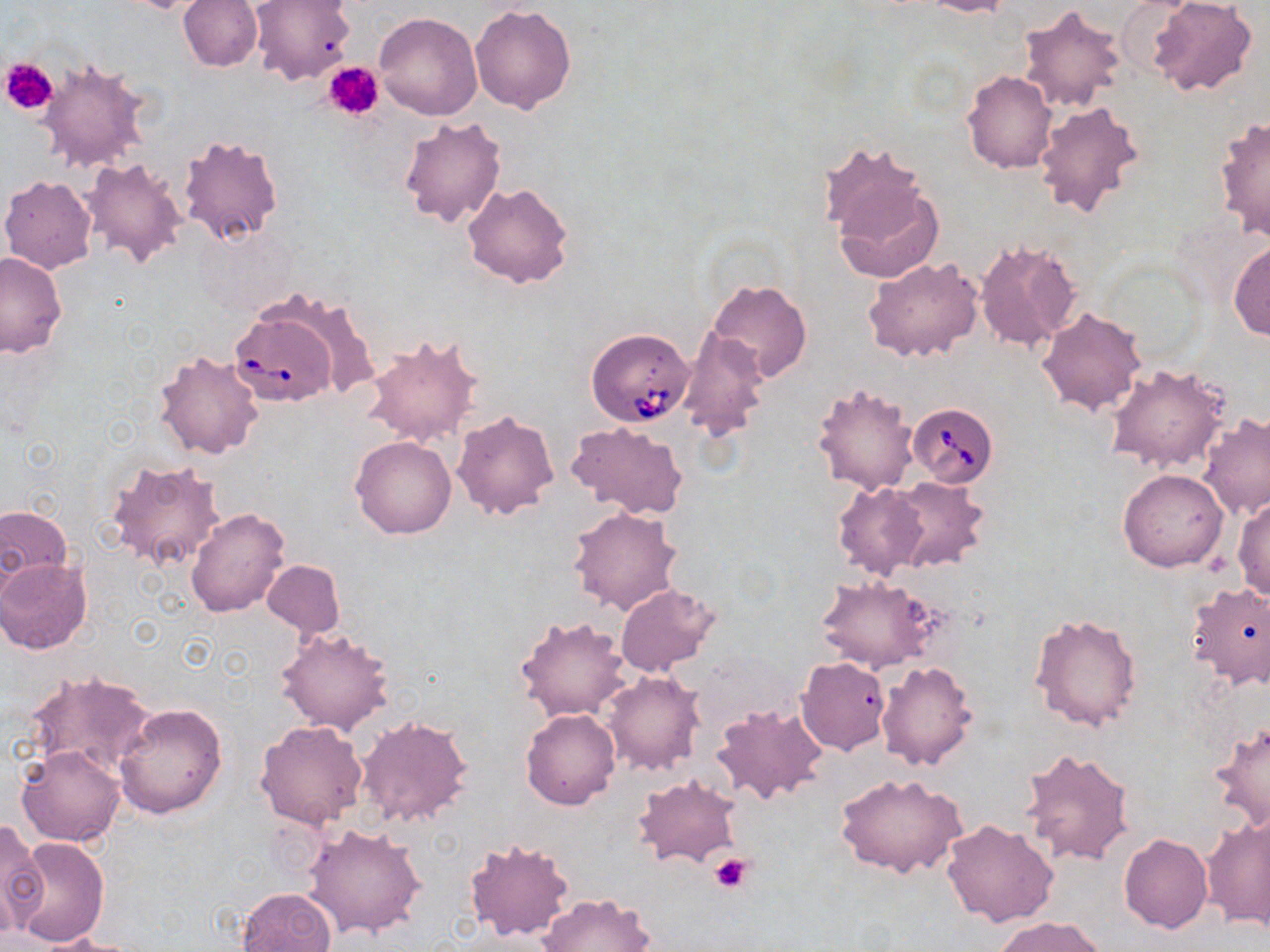 Approximate bounding boxes as (x1, y1, x2, y2) in pixels. Babesia divergens-infected red blood cell locations: (230, 307, 338, 408), (586, 327, 694, 429), (908, 402, 999, 487). Uninfected red blood cell locations: (178, 0, 261, 72), (251, 0, 357, 86), (922, 0, 1011, 17), (1115, 1, 1193, 74), (1148, 1, 1256, 97), (469, 4, 577, 113), (1016, 4, 1126, 114), (375, 11, 481, 120), (38, 59, 151, 173), (962, 71, 1056, 174), (1033, 99, 1144, 220), (398, 115, 507, 227), (1214, 117, 1269, 242), (178, 132, 285, 244), (827, 156, 943, 281), (81, 157, 189, 270), (0, 175, 98, 273), (462, 182, 574, 287), (975, 237, 1083, 353), (1228, 241, 1270, 341), (0, 251, 67, 358), (864, 257, 983, 364), (706, 278, 811, 384), (1036, 305, 1146, 416), (678, 330, 768, 440), (361, 333, 484, 448), (155, 348, 265, 460), (1104, 362, 1231, 475), (811, 380, 921, 495), (451, 409, 560, 521), (1198, 413, 1269, 521), (564, 421, 689, 519), (351, 435, 457, 539), (105, 456, 228, 573), (1118, 469, 1229, 571), (886, 476, 990, 574), (833, 481, 930, 580), (1234, 496, 1270, 600), (0, 503, 74, 589), (186, 506, 290, 618), (568, 506, 683, 615), (1, 557, 92, 652), (263, 560, 345, 636), (816, 574, 936, 671), (1185, 581, 1270, 688), (615, 585, 718, 677), (1030, 612, 1144, 732), (516, 615, 631, 721), (276, 626, 395, 736), (796, 657, 891, 755), (877, 660, 977, 771), (21, 669, 157, 777), (603, 671, 705, 775), (710, 702, 828, 806), (113, 703, 227, 819), (521, 710, 620, 810), (356, 714, 474, 830), (1210, 717, 1270, 834), (255, 719, 368, 828), (17, 745, 127, 849), (1020, 746, 1135, 867), (835, 772, 967, 879), (633, 774, 740, 867), (1203, 813, 1269, 928), (942, 818, 1060, 928), (0, 821, 47, 936), (304, 823, 428, 937), (1119, 833, 1212, 933), (11, 837, 109, 946), (464, 838, 576, 941), (237, 887, 338, 952), (537, 892, 655, 952), (993, 916, 1108, 952), (30, 933, 141, 952). Platelet locations: (1, 58, 57, 117), (324, 61, 383, 120), (708, 850, 753, 894). Slide-level diagnosis: Babesia divergens. 1000x magnification. One field of a larger specimen. Image is 1270×952 pixels. May-Grünwald-Giemsa stain. Thin blood smear. Light microscopy.